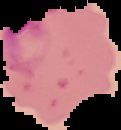

Result: malaria parasites detected. Cell region segmented out of the field of view; the surrounding area is masked to black. Image is 121×130 pixels. From a thin blood smear.